Assess the morphology of the red blood cells.
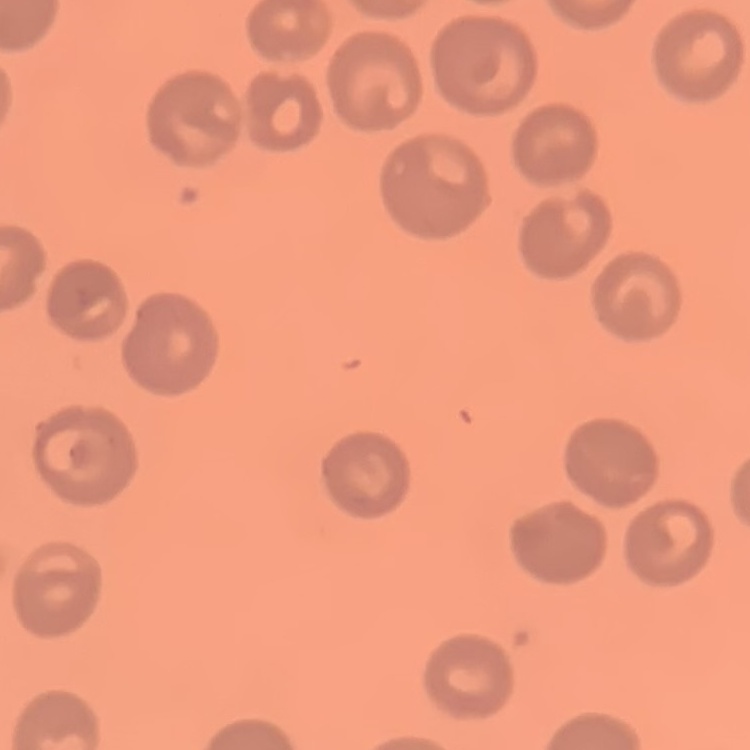

No rouleaux formation.

One tile cut from a larger photomicrograph. Thin blood smear. Stained with either Field's or Giemsa.